Locate every blood parasite and identify its species.
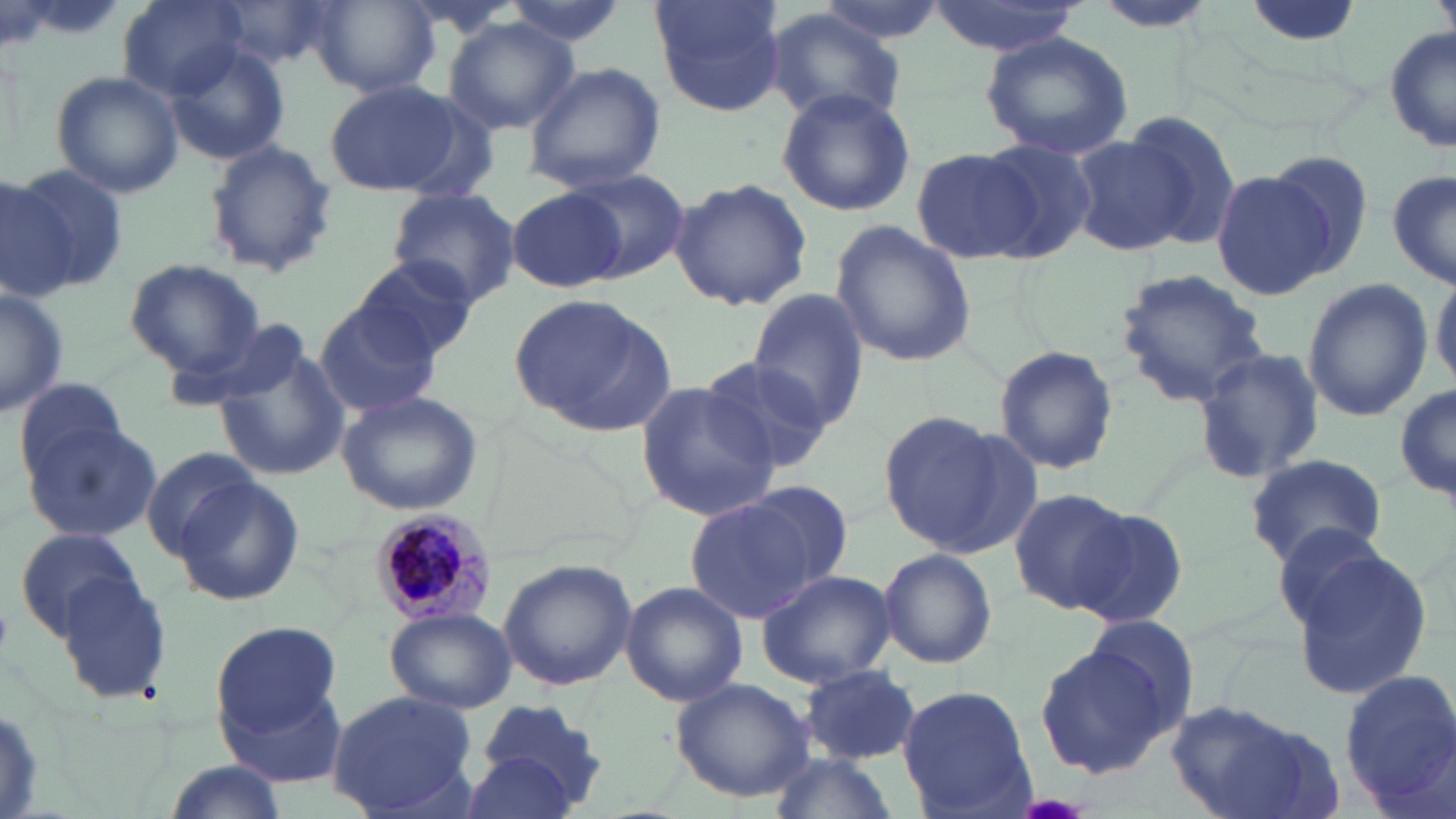

Approximate bounding boxes as (x1, y1, x2, y2) in pixels.
Plasmodium malariae-infected red blood cells: (371, 508, 494, 625).
No Plasmodium falciparum, Plasmodium ovale, Plasmodium vivax, Babesia divergens, or Trypanosoma brucei observed.

Uninfected red blood cell locations: (115, 0, 246, 99), (499, 0, 631, 49), (648, 0, 786, 117), (815, 0, 950, 45), (216, 1, 337, 70), (307, 1, 438, 97), (924, 1, 1088, 57), (1090, 2, 1223, 33), (764, 9, 909, 128), (443, 17, 580, 135), (1385, 24, 1456, 155), (982, 31, 1134, 159), (163, 40, 291, 165), (522, 62, 665, 191), (49, 69, 186, 199), (323, 80, 460, 196), (774, 88, 915, 216), (378, 91, 505, 199), (1116, 112, 1244, 248), (1069, 135, 1197, 254), (971, 137, 1097, 264), (203, 140, 337, 280), (911, 147, 1038, 265), (1263, 149, 1377, 279), (4, 160, 129, 296), (1208, 168, 1336, 300), (1389, 168, 1456, 291), (558, 169, 691, 281), (0, 173, 65, 300), (669, 176, 812, 312), (387, 187, 520, 307), (507, 187, 627, 293), (828, 220, 977, 368), (348, 255, 478, 365), (123, 258, 265, 376), (1113, 268, 1271, 408), (1430, 269, 1456, 389), (1303, 279, 1432, 423), (0, 286, 67, 419), (747, 289, 872, 433), (508, 294, 672, 431), (312, 298, 444, 420), (175, 315, 320, 413), (215, 342, 351, 486), (993, 345, 1119, 476), (1190, 349, 1325, 483), (696, 352, 838, 474), (10, 375, 134, 488), (632, 379, 781, 524), (1394, 384, 1454, 510), (336, 389, 484, 515), (874, 410, 1005, 548), (25, 416, 161, 543), (140, 446, 262, 561), (1243, 453, 1387, 568), (175, 477, 305, 606), (739, 477, 858, 583), (1008, 487, 1133, 613), (687, 498, 821, 621), (1071, 505, 1190, 631), (1268, 515, 1397, 642), (13, 526, 140, 641), (1284, 545, 1432, 699), (878, 547, 997, 669), (498, 559, 638, 690), (757, 568, 895, 687), (57, 572, 172, 705), (620, 580, 747, 707), (385, 608, 517, 713), (1084, 616, 1199, 726), (212, 621, 345, 735), (1034, 642, 1173, 778), (800, 665, 921, 764), (1340, 668, 1456, 805), (669, 676, 817, 802), (222, 685, 349, 789), (897, 685, 1033, 816), (327, 690, 480, 817), (1169, 701, 1331, 819), (466, 703, 611, 817), (762, 749, 896, 819), (160, 758, 291, 819). Slide-level diagnosis: Plasmodium malariae. Light microscopy. Image is 1456×819 pixels. Thin blood film. May-Grünwald-Giemsa stain. Single field of view. Captured at 1000x magnification.